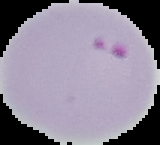

Image is 160×145 pixels. Segmented cell region on a black background. From a thin blood film. Malaria status: parasitized.